Assess this cell for malaria.
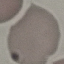

It is uninfected.

Giemsa stain. Thin blood smear. Acquired by smartphone through the microscope eyepiece. Cell patch, automatically extracted from a larger field of view and resized to 64 × 64 pixels.